Give a bounding box for every leukocyte visible.
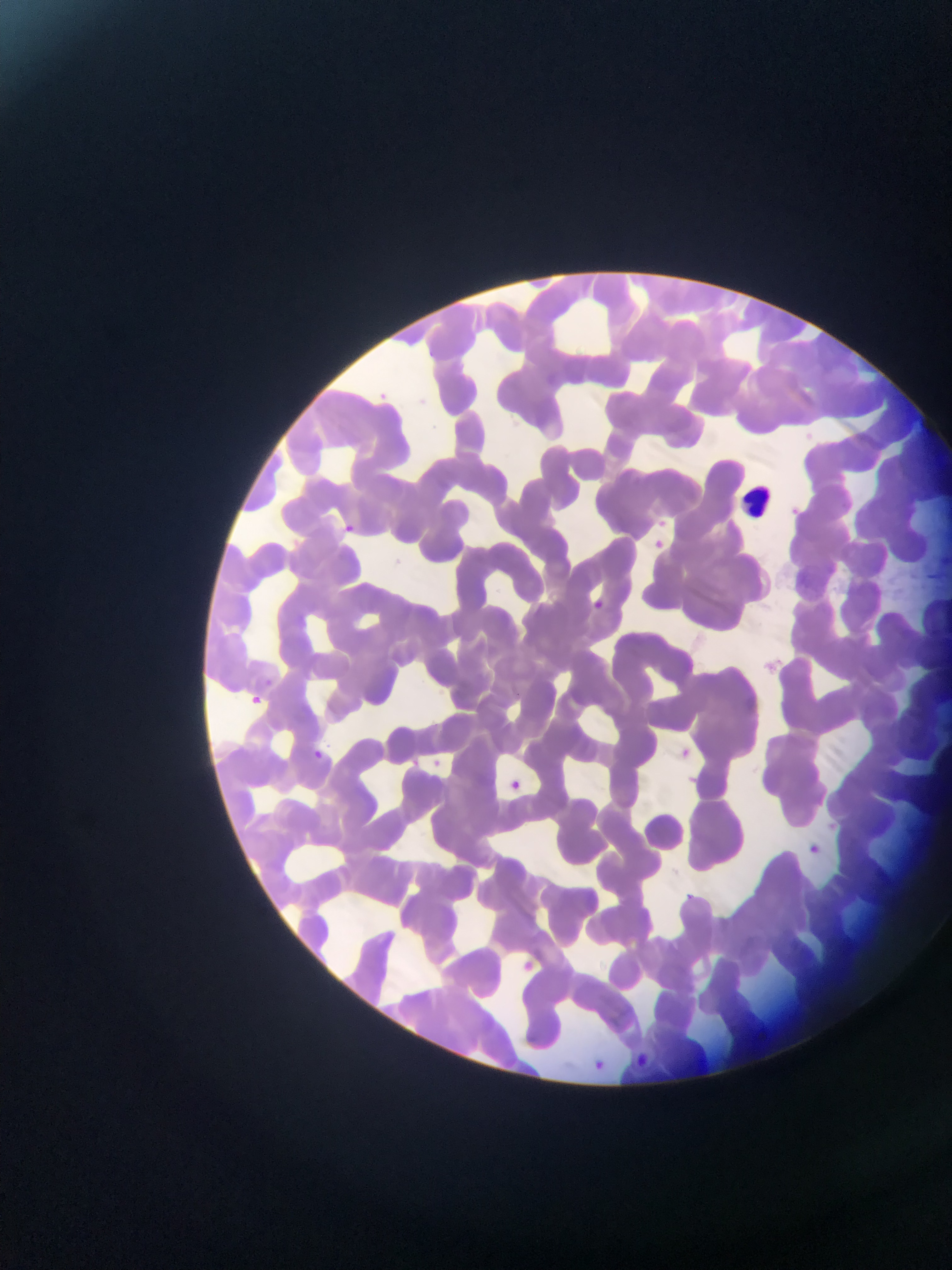
Approximate bounding boxes as [left, top, right, bottom] in pixels.
Leukocytes: [740, 479, 778, 519].

Plasmodium parasite locations: [658, 513, 670, 531], [342, 522, 362, 544], [654, 536, 666, 556], [589, 596, 606, 616], [264, 672, 281, 689], [245, 694, 272, 714], [681, 741, 700, 754], [312, 745, 326, 765], [425, 752, 445, 766], [509, 775, 528, 792], [822, 811, 835, 834], [800, 834, 823, 857], [684, 888, 694, 906], [519, 953, 540, 977], [629, 1045, 652, 1076], [592, 1054, 626, 1078]. Mobile-phone photograph taken through the microscope. Image is 952×1270 pixels. Collected in Ghana. One field of view. Thin blood smear.